Identify the preparation type.
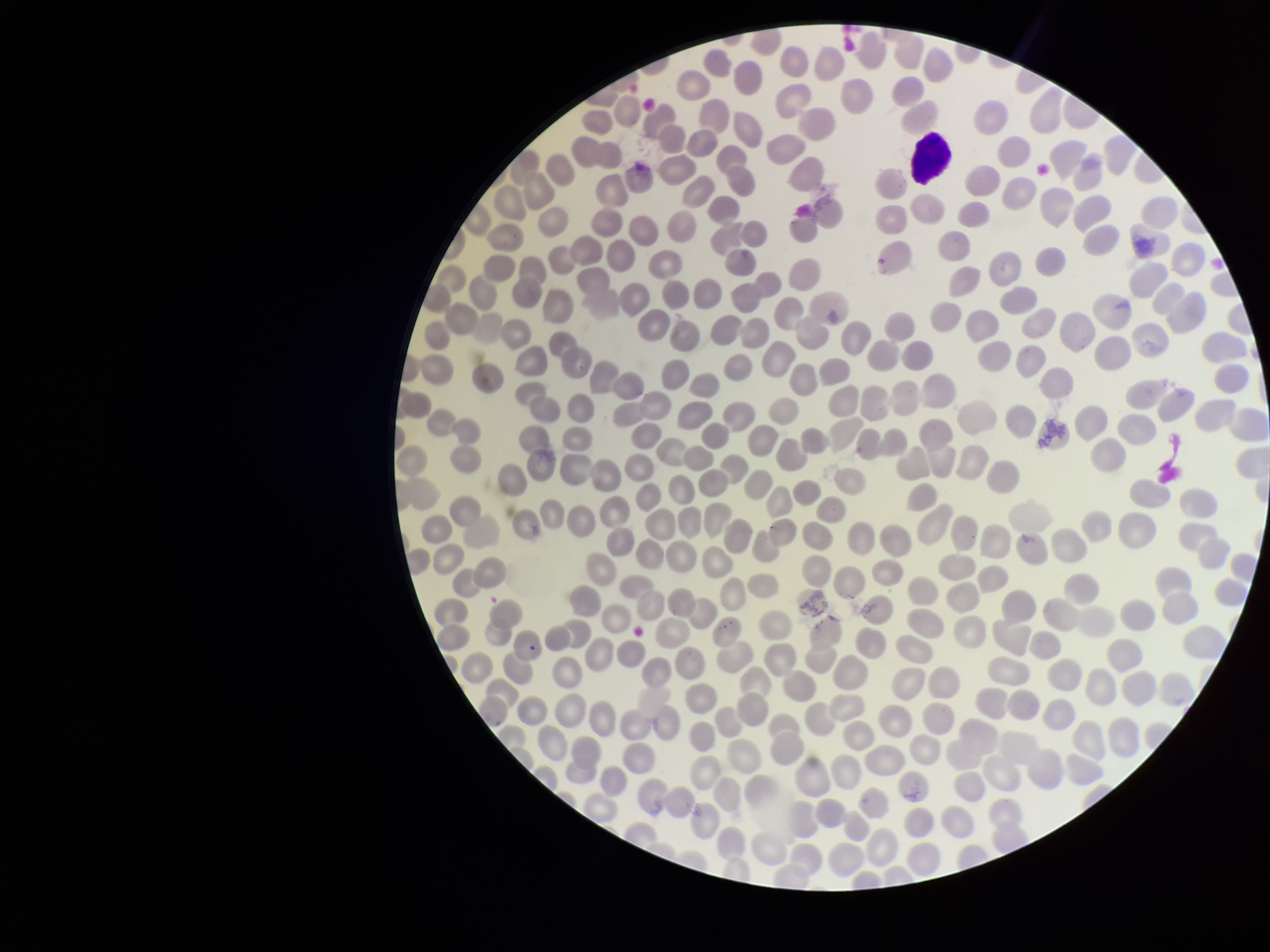
Thin.

Summary:
  - Parasitized red blood cell count: 0
  - Image size: 1270×952 pixels
  - Stain: Giemsa
  - Red blood cell count: 294
  - Capture: smartphone photograph through the microscope eyepiece
  - Parasitized red blood cells: none identified
  - Field of view: single
  - Patient malaria status: negative